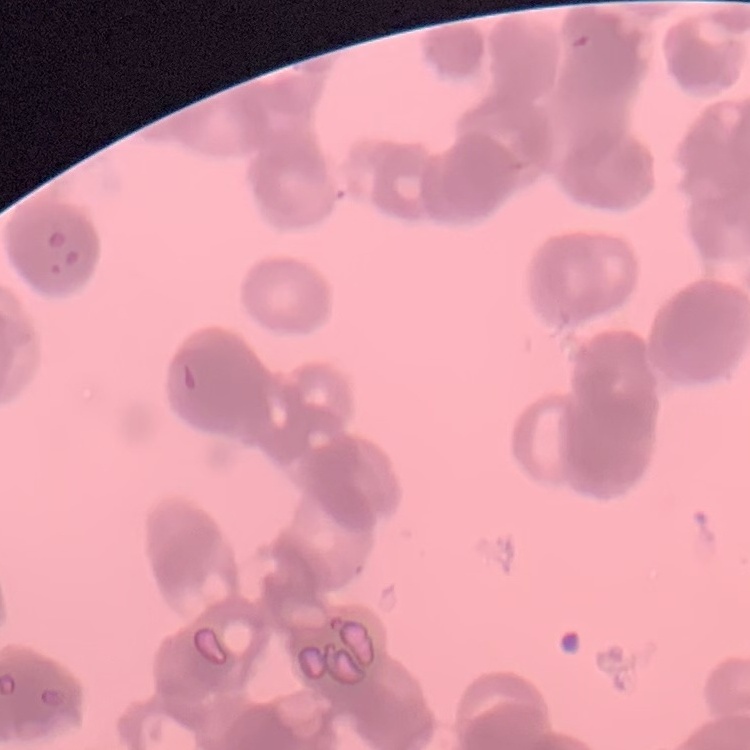
The red blood cells exhibit rouleaux formation. Thin blood film. Stained with either Field's or Giemsa. Square crop of a larger photomicrograph.